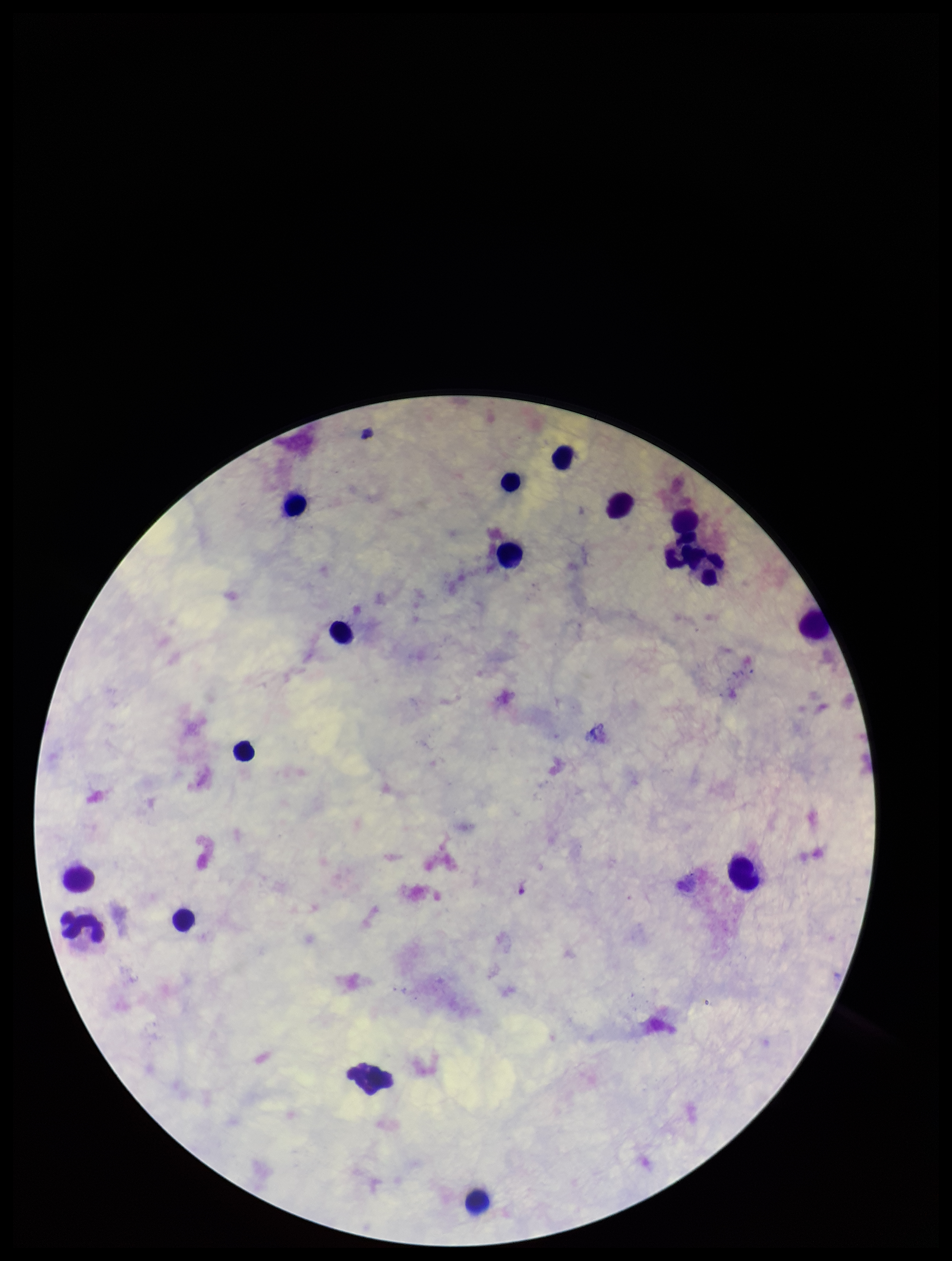

One field from this slide. Image is 952×1261 pixels. Patient malaria status: negative. Smartphone photograph taken through the eyepiece of a microscope. Parasite count: 0. Giemsa stain. Leukocyte count: 16. Preparation: thick blood smear. Plasmodium parasites: none identified.